Assess this cell for malaria.
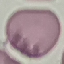

It is uninfected.

{
  "stain": "Giemsa",
  "image_type": "cell patch, automatically extracted from a larger field of view and resized to 64 × 64 pixels",
  "capture": "smartphone through the microscope eyepiece",
  "preparation": "thin blood smear"
}